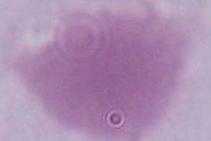

Summary:
  - Magnification: 1000x
  - Modality: micrograph
  - Identification: red blood cell